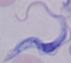

Photomicrograph. 1000x magnification. A trypanosome is shown.